Locate every Plasmodium ovale-infected red blood cell.
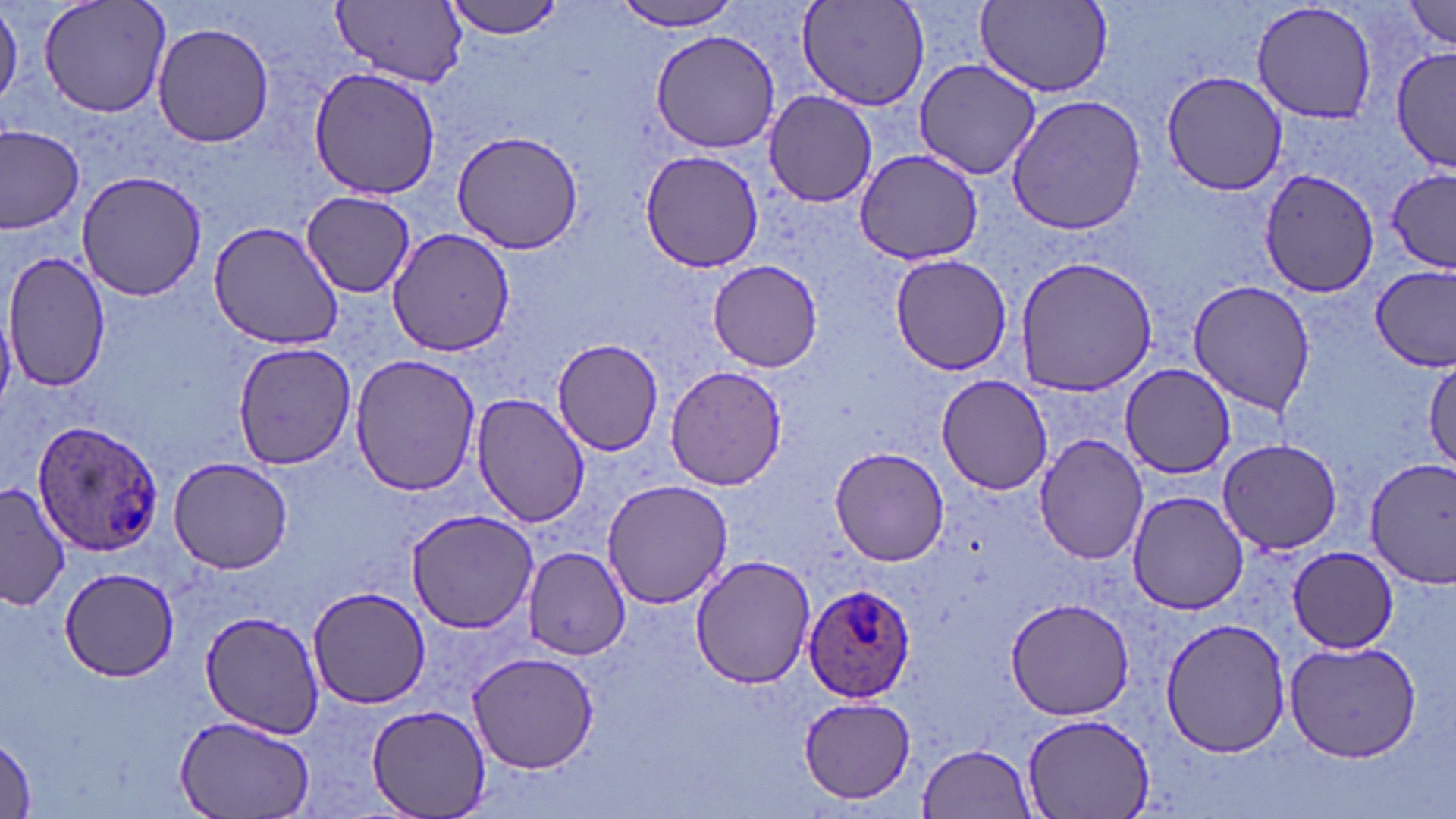

Approximate bounding boxes as (x1, y1, x2, y2) in pixels.
Plasmodium ovale-infected red blood cells: (30, 421, 165, 556), (801, 587, 915, 704).

{
  "slide_level_diagnosis": "Plasmodium ovale",
  "image_size": "1456×819 pixels",
  "uninfected_red_blood_cell_locations": "approximate bounding boxes as (x1, y1, x2, y2) in pixels: (0, 0, 22, 112), (39, 0, 171, 120), (441, 0, 567, 40), (332, 1, 467, 86), (612, 1, 750, 32), (798, 1, 930, 112), (976, 1, 1114, 95), (1249, 1, 1381, 123), (1405, 2, 1456, 51), (152, 21, 274, 148), (648, 28, 784, 154), (1395, 47, 1456, 169), (912, 58, 1042, 179), (308, 65, 443, 199), (1158, 70, 1290, 195), (763, 90, 880, 208), (1006, 95, 1147, 234), (0, 127, 86, 233), (450, 129, 586, 255), (854, 147, 982, 264), (638, 149, 766, 272), (1260, 166, 1381, 297), (76, 169, 205, 302), (1384, 171, 1456, 273), (300, 189, 418, 295), (210, 219, 346, 350), (387, 226, 517, 356), (4, 251, 112, 393), (889, 252, 1014, 376), (1015, 256, 1156, 396), (708, 259, 824, 372), (1371, 265, 1456, 372), (1188, 279, 1316, 415), (549, 339, 666, 456), (231, 343, 358, 468), (349, 353, 480, 496), (1426, 358, 1456, 472), (665, 363, 786, 490), (1120, 363, 1237, 478), (936, 374, 1054, 494), (471, 393, 589, 528), (1035, 434, 1150, 566), (1219, 439, 1342, 553), (828, 445, 952, 567), (168, 456, 294, 573), (1367, 457, 1456, 588), (600, 479, 733, 611), (0, 480, 73, 611), (1125, 491, 1251, 614), (407, 507, 538, 633), (1287, 545, 1400, 653), (523, 546, 630, 660), (690, 553, 816, 687), (59, 567, 179, 681), (305, 587, 432, 709), (1004, 597, 1135, 719), (201, 611, 328, 737), (1161, 616, 1291, 759), (1284, 639, 1424, 763), (466, 649, 601, 773), (798, 695, 918, 803), (367, 706, 489, 818), (1020, 714, 1153, 819), (175, 716, 316, 819), (1, 736, 37, 819), (920, 743, 1037, 818)",
  "stain": "May-Grünwald-Giemsa",
  "magnification": "1000x",
  "preparation": "thin blood smear",
  "field_of_view": "single",
  "modality": "light microscopy"
}